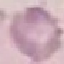
Malaria status: uninfected. Automatically extracted cell patch, resized to 64 × 64 pixels. Acquired by smartphone through the microscope eyepiece. Giemsa stain. Thin blood smear.